Locate every blood parasite and identify its species.
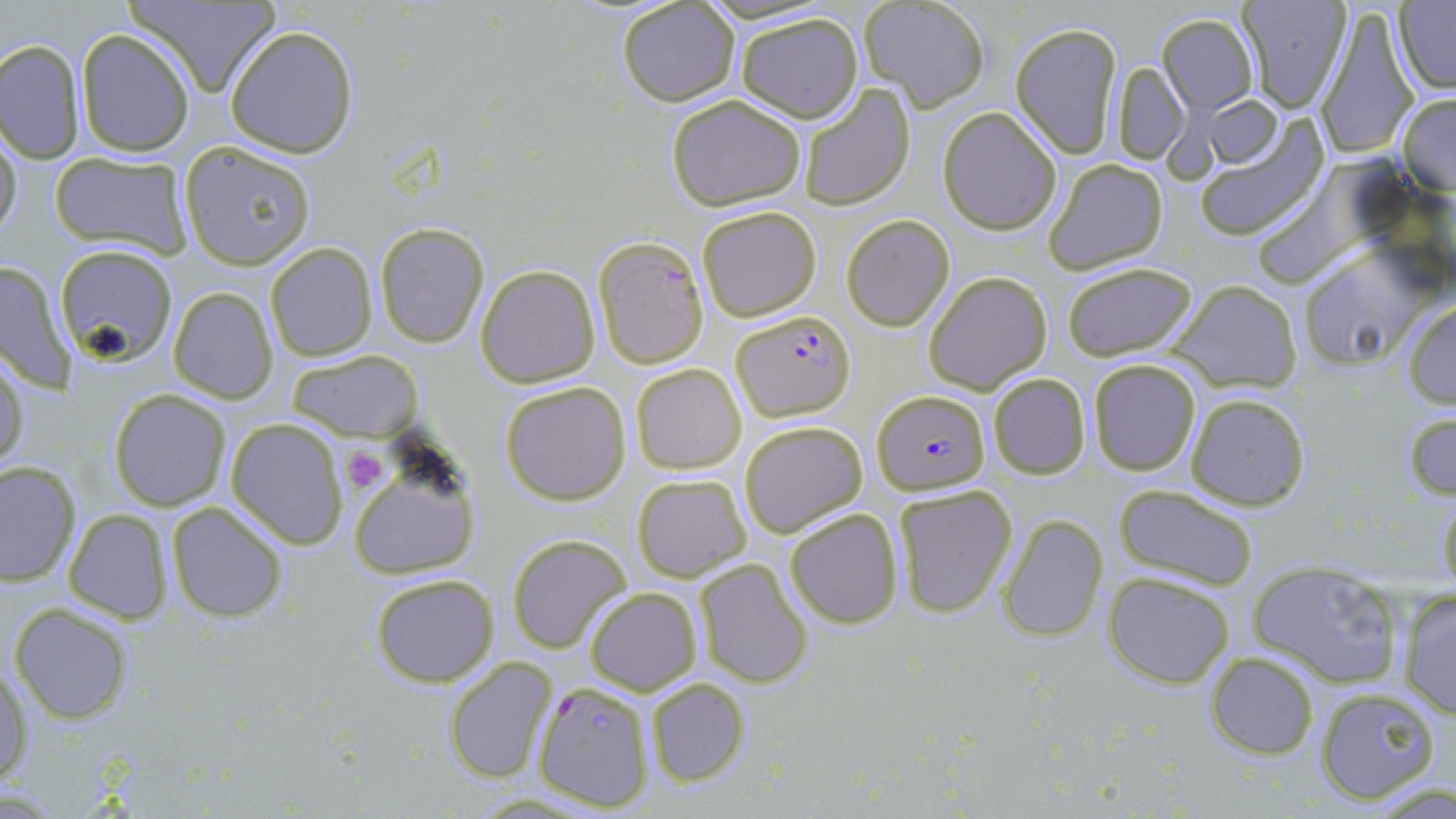

Approximate bounding boxes as (x1, y1, x2, y2) in pixels.
Plasmodium falciparum-infected red blood cells: (731, 308, 855, 420), (872, 388, 989, 495), (534, 681, 656, 813).
No Plasmodium ovale, Plasmodium malariae, Plasmodium vivax, Babesia divergens, or Trypanosoma brucei observed.

slide-level diagnosis = Plasmodium falciparum
field of view = one of a larger specimen
stain = May-Grünwald-Giemsa
magnification = 1000x
modality = light microscopy
platelet locations = approximate bounding boxes as (x1, y1, x2, y2) in pixels: (342, 445, 390, 493)
image size = 1456×819 pixels
uninfected red blood cell locations = approximate bounding boxes as (x1, y1, x2, y2) in pixels: (121, 0, 281, 97), (858, 0, 992, 111), (1236, 0, 1351, 111), (1394, 1, 1455, 95), (616, 3, 740, 108), (1315, 4, 1418, 160), (733, 11, 864, 124), (1157, 12, 1257, 116), (1010, 20, 1123, 159), (225, 25, 360, 157), (75, 29, 194, 157), (0, 37, 85, 165), (1112, 62, 1188, 164), (799, 83, 916, 208), (1396, 92, 1456, 196), (664, 93, 809, 209), (1202, 94, 1282, 167), (938, 108, 1062, 236), (1190, 116, 1328, 242), (0, 123, 22, 246), (178, 142, 316, 270), (49, 153, 193, 258), (1041, 158, 1169, 276), (696, 205, 822, 321), (841, 214, 955, 331), (374, 223, 489, 348), (592, 236, 709, 369), (265, 242, 377, 363), (55, 244, 177, 365), (1297, 247, 1431, 370), (0, 258, 75, 393), (1060, 260, 1201, 364), (475, 265, 600, 387), (922, 271, 1052, 394), (1168, 279, 1302, 394), (168, 286, 279, 404), (1403, 300, 1456, 409), (0, 346, 30, 476), (287, 350, 421, 443), (1087, 357, 1203, 476), (629, 364, 747, 475), (987, 372, 1091, 480), (498, 382, 632, 506), (109, 389, 231, 510), (1183, 391, 1311, 512), (1403, 409, 1456, 502), (225, 418, 349, 548), (738, 420, 868, 539), (0, 461, 80, 588), (350, 461, 480, 580), (632, 473, 752, 584), (891, 483, 1019, 618), (1433, 483, 1456, 591), (1112, 485, 1261, 592), (165, 501, 289, 624), (785, 508, 904, 628), (62, 509, 174, 624), (997, 513, 1109, 642), (507, 533, 631, 653), (692, 558, 813, 688), (1249, 562, 1406, 689), (1102, 570, 1236, 689), (370, 573, 499, 688), (1396, 586, 1456, 719), (584, 587, 702, 696), (10, 603, 135, 723), (1204, 650, 1320, 760), (444, 658, 558, 785), (1, 659, 30, 786), (644, 678, 750, 787), (1313, 684, 1445, 805)
preparation = thin blood smear